Point out each Plasmodium parasite.
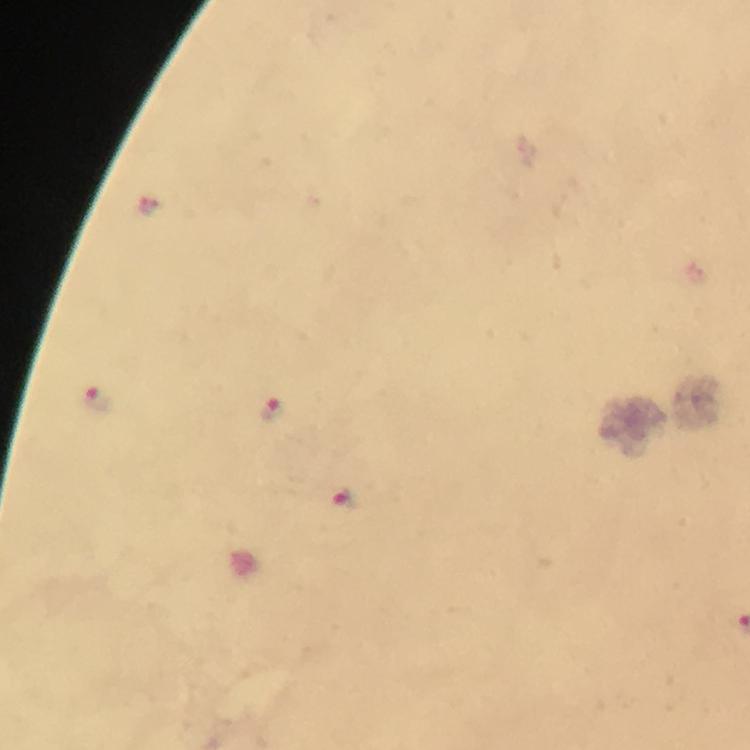
Approximate centers as [x, y] in pixels.
Plasmodium parasites: [96, 400], [272, 410], [345, 498].

Summary:
  - Immersion oil: applied
  - Stain: Giemsa
  - Capture: smartphone camera through the microscope
  - Preparation: thick smear
  - Context: from a diagnostic examination for malaria
  - Cropped from: one field of view
  - Magnification: 100x
  - Image size: 750×750 pixels